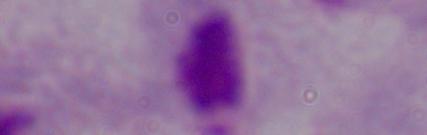
Summary:
  - Magnification: 1000x
  - Identification: trichomonad
  - Modality: micrograph